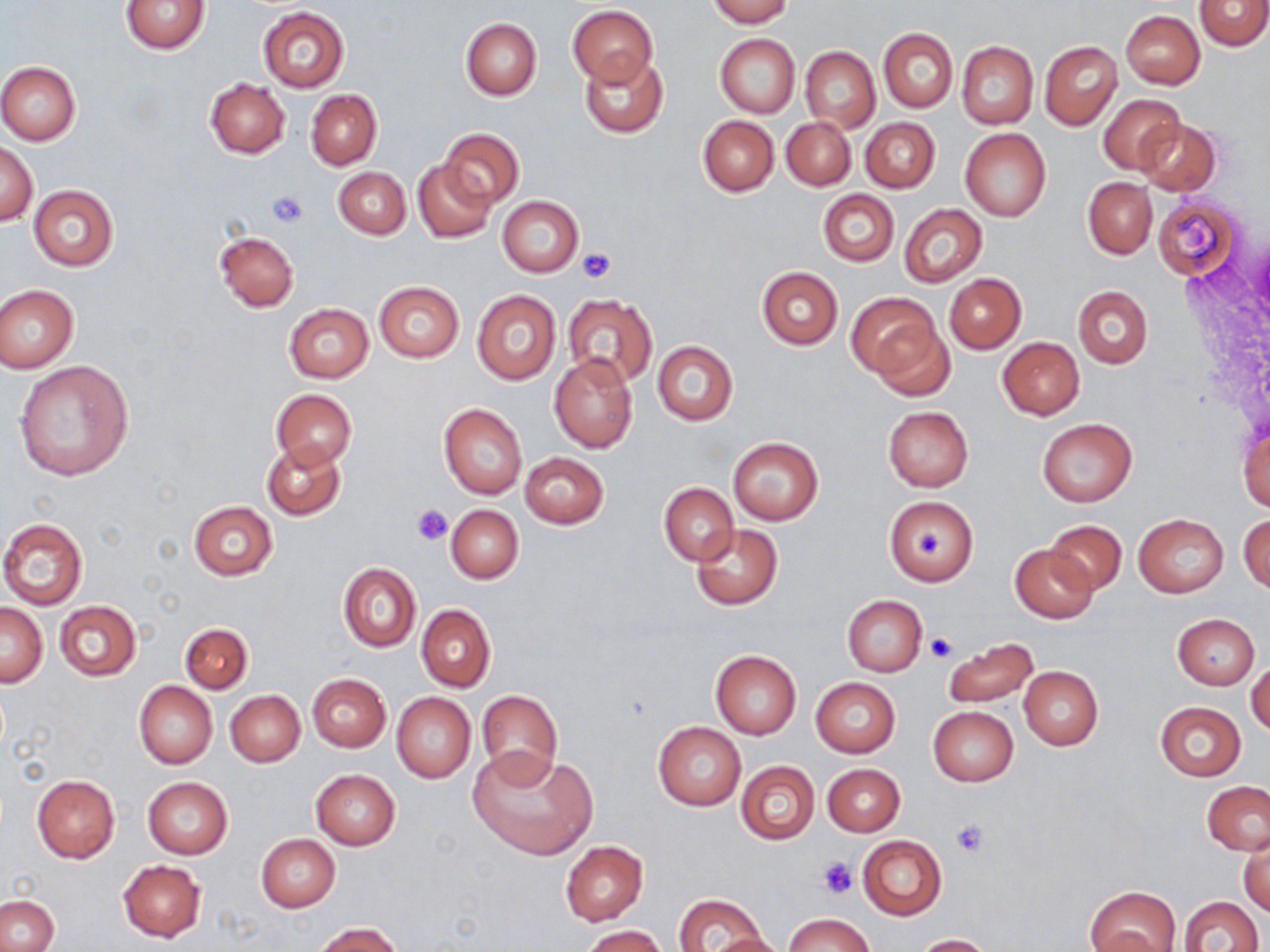
slide-level diagnosis = negative for blood parasites
stain = May-Grünwald-Giemsa
preparation = thin blood smear
uninfected red blood cell locations = approximate bounding boxes as (x1,y1)-(x2,y2) corner pairs in pixels: (705,0)-(793,26), (1194,0)-(1270,50), (120,1)-(210,54), (568,4)-(658,86), (258,6)-(348,91), (1120,10)-(1204,90), (461,18)-(542,100), (878,28)-(957,112), (715,34)-(799,118), (1039,40)-(1121,130), (955,41)-(1037,128), (800,46)-(880,132), (579,52)-(668,138), (0,61)-(81,144), (204,77)-(290,158), (306,89)-(381,170), (1098,94)-(1185,174), (697,116)-(778,196), (781,117)-(857,190), (861,118)-(939,192), (1135,118)-(1222,196), (438,128)-(524,208), (959,128)-(1051,222), (1,141)-(37,225), (413,160)-(497,243), (333,167)-(411,239), (1083,178)-(1156,259), (28,185)-(119,270), (817,189)-(899,267), (498,196)-(583,276), (1152,196)-(1242,278), (898,203)-(987,287), (215,231)-(298,311), (756,267)-(842,350), (944,273)-(1025,354), (373,281)-(464,362), (0,284)-(79,372), (1072,285)-(1153,370), (471,291)-(561,384), (847,292)-(943,381), (562,294)-(657,386), (283,303)-(374,383), (867,316)-(956,402), (997,337)-(1085,419), (653,342)-(738,424), (548,353)-(638,453), (13,360)-(133,481), (271,388)-(355,469), (438,401)-(527,499), (883,406)-(973,491), (1035,418)-(1137,508), (1238,423)-(1270,514), (728,437)-(823,524), (260,439)-(346,520), (520,452)-(609,530), (659,483)-(738,566), (884,495)-(978,585), (188,501)-(278,579), (445,505)-(523,583), (1239,512)-(1269,592), (1133,514)-(1229,598), (0,517)-(88,609), (1045,519)-(1126,594), (690,524)-(782,610), (1010,544)-(1097,622), (337,562)-(420,652), (842,594)-(926,678), (54,600)-(141,682), (0,603)-(47,686), (416,604)-(496,692), (1173,613)-(1259,690), (180,623)-(252,693), (943,637)-(1038,708), (710,650)-(802,738), (1247,656)-(1270,736), (1018,666)-(1103,750), (307,673)-(390,752), (811,678)-(900,757), (134,681)-(217,770), (476,689)-(563,785), (225,690)-(304,767), (391,692)-(476,782), (1156,701)-(1245,780), (927,707)-(1017,787), (653,720)-(745,810), (468,745)-(599,861), (735,760)-(819,845), (822,763)-(904,836), (311,769)-(400,850), (31,776)-(119,863), (142,777)-(233,858), (1201,781)-(1270,856), (256,833)-(341,912), (1239,834)-(1269,916), (857,835)-(947,920), (560,841)-(647,925), (118,860)-(207,942), (1085,885)-(1182,952), (674,893)-(769,952), (1,896)-(57,952), (1177,896)-(1264,952), (785,913)-(871,952), (312,923)-(405,952), (581,925)-(669,952), (708,932)-(787,952), (913,934)-(997,951)
image size = 1270×952 pixels
field of view = single
modality = light microscopy
magnification = 1000x
platelet locations = approximate bounding boxes as (x1,y1)-(x2,y2) corner pairs in pixels: (267,192)-(307,228), (577,248)-(616,283), (412,505)-(453,546), (913,531)-(941,557), (926,631)-(956,662), (950,820)-(988,858), (816,856)-(858,898)